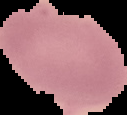
preparation = thin blood film
result = no malaria parasites detected
image type = cell region segmented out of the field of view; surrounding area masked to black
image size = 127×115 pixels